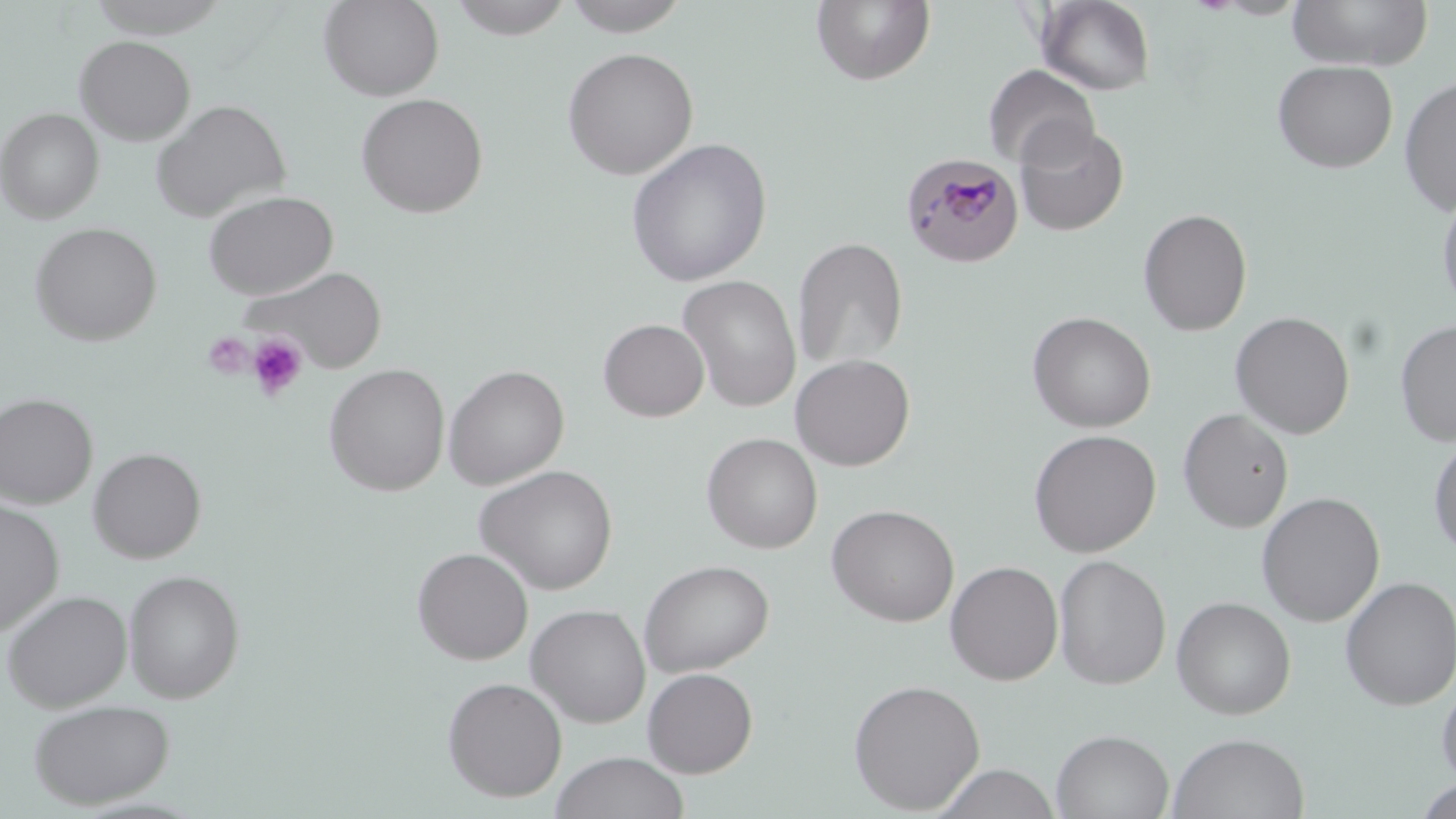
slide-level diagnosis = Plasmodium malariae
image size = 1456×819 pixels
stain = May-Grünwald-Giemsa
modality = optical microscopy
preparation = thin blood smear
uninfected red blood cell locations = approximate bounding boxes as named x1/y1/x2/y2 corners in pixels: (x1=87, y1=0, x2=231, y2=38), (x1=318, y1=0, x2=444, y2=101), (x1=447, y1=0, x2=575, y2=39), (x1=561, y1=0, x2=692, y2=37), (x1=811, y1=0, x2=936, y2=86), (x1=1287, y1=0, x2=1433, y2=71), (x1=1037, y1=1, x2=1156, y2=95), (x1=74, y1=35, x2=196, y2=145), (x1=562, y1=46, x2=699, y2=180), (x1=1272, y1=60, x2=1398, y2=173), (x1=984, y1=63, x2=1100, y2=171), (x1=1399, y1=76, x2=1456, y2=216), (x1=355, y1=92, x2=488, y2=218), (x1=150, y1=99, x2=289, y2=222), (x1=0, y1=108, x2=103, y2=223), (x1=1014, y1=122, x2=1129, y2=237), (x1=625, y1=138, x2=772, y2=287), (x1=1437, y1=188, x2=1456, y2=317), (x1=202, y1=190, x2=339, y2=300), (x1=1138, y1=208, x2=1252, y2=336), (x1=29, y1=222, x2=162, y2=346), (x1=792, y1=237, x2=908, y2=369), (x1=242, y1=265, x2=388, y2=372), (x1=678, y1=274, x2=802, y2=412), (x1=1027, y1=311, x2=1156, y2=433), (x1=1229, y1=311, x2=1356, y2=439), (x1=598, y1=318, x2=709, y2=422), (x1=1395, y1=319, x2=1456, y2=448), (x1=791, y1=353, x2=915, y2=471), (x1=323, y1=363, x2=450, y2=496), (x1=444, y1=365, x2=569, y2=490), (x1=0, y1=392, x2=97, y2=508), (x1=1177, y1=408, x2=1294, y2=532), (x1=1028, y1=428, x2=1162, y2=558), (x1=701, y1=432, x2=822, y2=554), (x1=1428, y1=432, x2=1456, y2=559), (x1=88, y1=447, x2=206, y2=563), (x1=474, y1=465, x2=619, y2=595), (x1=1256, y1=491, x2=1386, y2=627), (x1=0, y1=499, x2=64, y2=636), (x1=826, y1=504, x2=960, y2=627), (x1=412, y1=547, x2=534, y2=665), (x1=1052, y1=554, x2=1171, y2=690), (x1=639, y1=559, x2=774, y2=677), (x1=945, y1=560, x2=1063, y2=685), (x1=123, y1=569, x2=245, y2=703), (x1=1339, y1=576, x2=1456, y2=710), (x1=2, y1=589, x2=132, y2=711), (x1=1171, y1=596, x2=1296, y2=720), (x1=526, y1=603, x2=651, y2=728), (x1=642, y1=667, x2=758, y2=777), (x1=1436, y1=675, x2=1456, y2=790), (x1=442, y1=677, x2=567, y2=802), (x1=847, y1=678, x2=985, y2=814), (x1=28, y1=698, x2=175, y2=809), (x1=1052, y1=728, x2=1174, y2=819), (x1=1168, y1=732, x2=1310, y2=819), (x1=550, y1=751, x2=690, y2=819), (x1=933, y1=763, x2=1061, y2=819), (x1=1414, y1=778, x2=1456, y2=819)
Plasmodium malariae-infected red blood cell locations = approximate bounding boxes as named x1/y1/x2/y2 corners in pixels: (x1=901, y1=152, x2=1024, y2=268)
magnification = 1000x
field of view = one of a larger specimen
platelet locations = approximate bounding boxes as named x1/y1/x2/y2 corners in pixels: (x1=203, y1=331, x2=254, y2=378), (x1=246, y1=334, x2=307, y2=403)